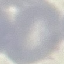 Malaria status: uninfected. Photographed with a smartphone camera at the microscope eyepiece. Giemsa-stained preparation. Thin blood smear. Automatically extracted cell patch, resized to 64 × 64 pixels.